Classify this cell by malaria status.
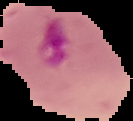

Parasitized.

From a thin blood smear. Segmented cell region on a black background. Image is 133×121 pixels.